Outline each Plasmodium falciparum-infected red blood cell.
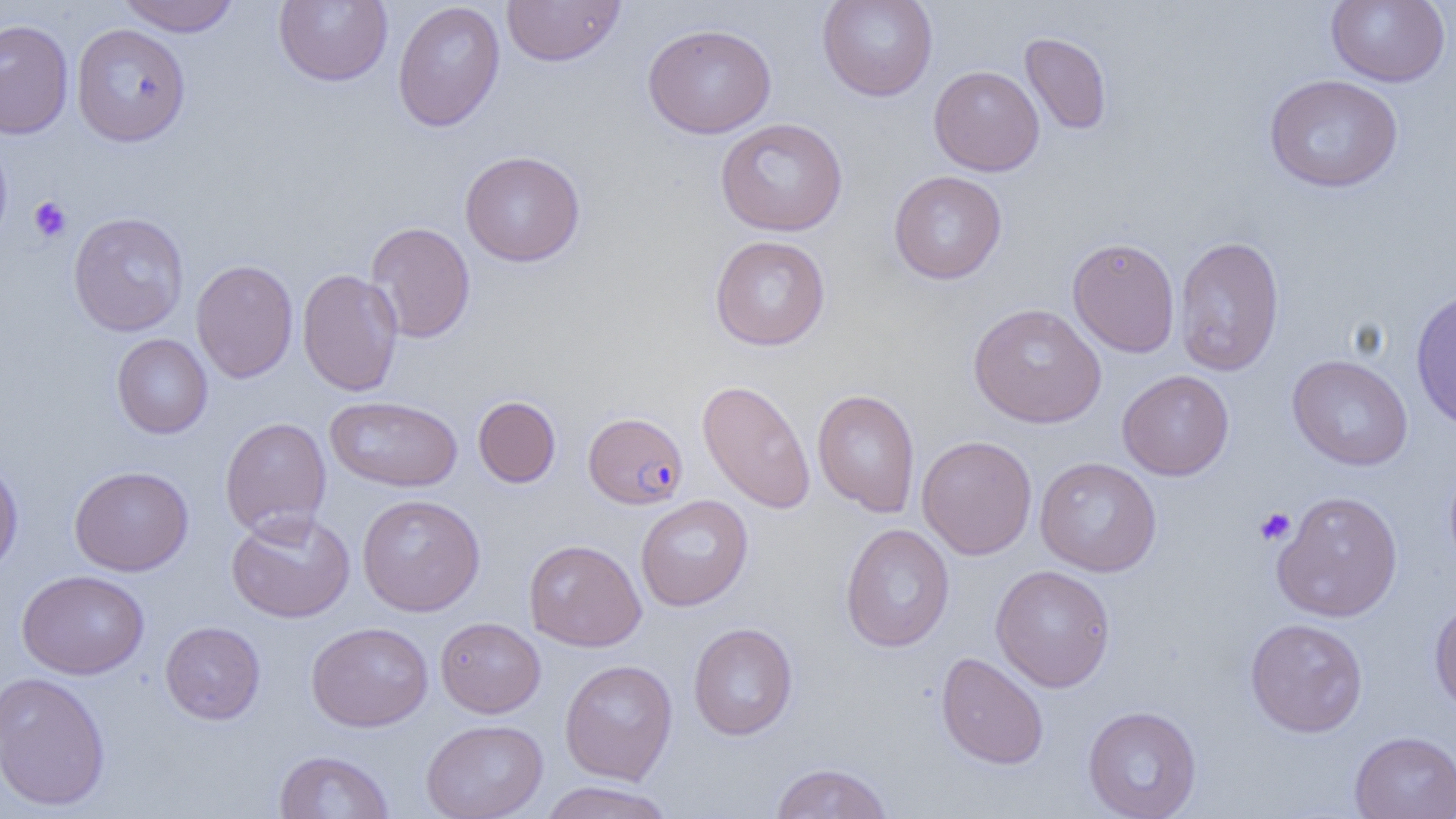
Approximate bounding boxes as [x1, y1, x2, y2] in pixels.
Plasmodium falciparum-infected red blood cells: [583, 411, 689, 509].

Uninfected red blood cell locations: [115, 0, 241, 36], [274, 0, 393, 87], [502, 0, 626, 67], [816, 0, 938, 101], [1325, 0, 1450, 87], [392, 1, 505, 132], [0, 19, 74, 138], [71, 23, 191, 146], [642, 23, 777, 139], [1020, 32, 1113, 135], [928, 65, 1044, 176], [1263, 74, 1403, 193], [715, 118, 847, 236], [0, 134, 13, 250], [460, 150, 585, 267], [888, 170, 1007, 284], [68, 211, 190, 337], [365, 222, 476, 343], [709, 235, 831, 351], [1173, 235, 1285, 376], [1067, 237, 1181, 358], [190, 259, 299, 383], [297, 268, 404, 396], [1410, 288, 1456, 432], [968, 303, 1106, 428], [112, 334, 212, 439], [1286, 355, 1413, 471], [1117, 370, 1234, 480], [697, 379, 815, 514], [812, 389, 920, 517], [325, 395, 463, 493], [473, 396, 561, 488], [220, 417, 332, 538], [917, 435, 1038, 560], [0, 456, 23, 579], [1034, 457, 1162, 577], [1443, 459, 1456, 580], [69, 465, 194, 576], [1272, 490, 1403, 622], [357, 494, 485, 616], [635, 495, 753, 612], [225, 510, 356, 623], [840, 523, 955, 652], [524, 539, 646, 651], [990, 565, 1116, 692], [17, 569, 149, 679], [1429, 595, 1456, 718], [435, 617, 546, 718], [1244, 618, 1368, 737], [160, 621, 265, 724], [306, 621, 434, 732], [688, 623, 798, 740], [935, 652, 1049, 769], [559, 659, 678, 784], [0, 671, 111, 811], [1083, 705, 1202, 819], [421, 718, 548, 819], [1349, 731, 1456, 818], [274, 750, 395, 818], [769, 761, 894, 819], [537, 780, 676, 819]. Platelet locations: [29, 196, 72, 242], [1253, 507, 1296, 546]. Slide-level diagnosis: Plasmodium falciparum. Image is 1456×819 pixels. Thin blood smear. 1000x magnification. Optical microscopy. Single field of view.